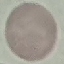

result = negative for malaria parasites
stain = Giemsa
capture = smartphone through the microscope eyepiece
preparation = thin smear
image type = automatically extracted cell patch, resized to 64 × 64 pixels